Report the malaria status of this cell.
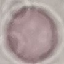
It is uninfected.

Giemsa-stained preparation. Acquired by smartphone through the microscope eyepiece. Thin blood smear. Automatically extracted cell patch, resized to 64 × 64 pixels.